Give the extent of all Babesia divergens-infected red blood cells.
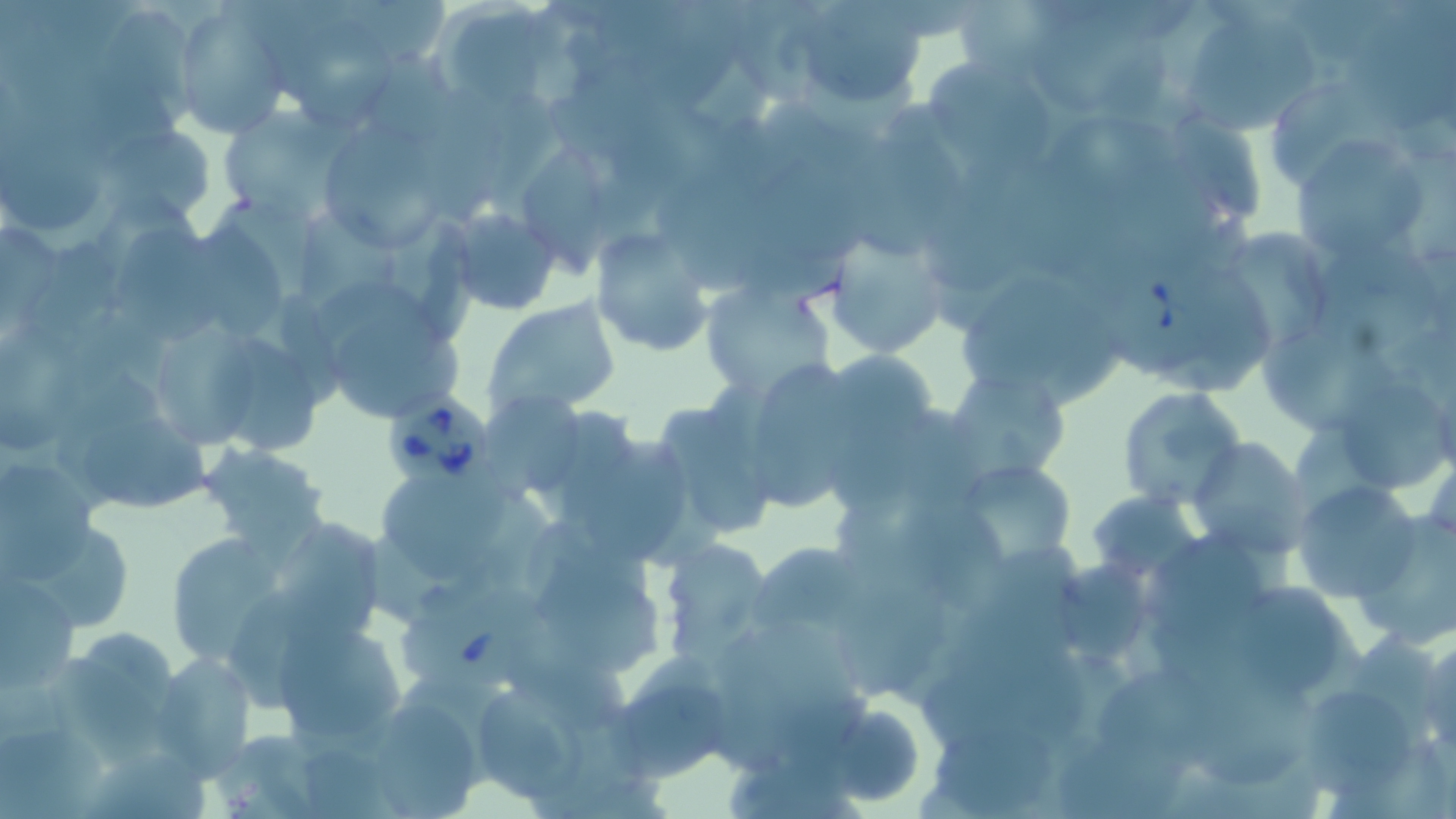

Approximate bounding boxes as (x1,y1)-(x2,y2) corner pairs in pixels.
Babesia divergens-infected red blood cells: (1097,249)-(1228,380), (384,386)-(497,495), (397,590)-(564,698).

Uninfected red blood cell locations: (788,1)-(930,111), (170,2)-(294,138), (433,2)-(565,110), (1181,4)-(1323,133), (102,6)-(203,132), (1038,18)-(1151,108), (277,19)-(405,128), (931,57)-(1055,178), (1272,79)-(1410,198), (218,106)-(340,225), (326,116)-(439,245), (103,123)-(219,228), (1288,135)-(1434,266), (521,144)-(611,284), (440,203)-(563,316), (300,207)-(399,347), (385,212)-(478,344), (118,224)-(219,347), (825,225)-(955,360), (589,228)-(718,359), (1237,228)-(1333,348), (1312,242)-(1446,355), (964,272)-(1095,390), (701,279)-(835,400), (484,297)-(622,421), (335,316)-(466,417), (1256,326)-(1396,434), (3,330)-(91,451), (160,330)-(261,447), (208,337)-(318,455), (819,348)-(942,453), (734,356)-(865,514), (943,363)-(1073,484), (1343,380)-(1449,487), (1116,386)-(1247,511), (486,397)-(587,492), (648,401)-(779,544), (83,416)-(219,509), (584,434)-(692,563), (1187,437)-(1312,558), (197,444)-(331,554), (952,458)-(1080,573), (0,461)-(96,581), (1291,478)-(1425,604), (381,479)-(517,578), (1087,491)-(1203,581), (903,495)-(1008,613), (1351,512)-(1456,644), (284,523)-(394,641), (38,529)-(135,628), (160,532)-(289,671), (1145,535)-(1271,640), (658,536)-(775,664), (748,541)-(877,646), (1061,561)-(1155,660), (535,563)-(668,671), (0,572)-(80,694), (1239,580)-(1345,691), (838,581)-(952,698), (276,617)-(407,750), (1418,631)-(1456,753), (152,652)-(257,776), (53,654)-(168,759), (611,657)-(736,784), (1103,670)-(1228,784), (1189,678)-(1330,797), (1304,689)-(1413,801), (477,694)-(587,802), (816,702)-(928,807), (377,705)-(478,819), (931,720)-(1067,819), (0,725)-(103,819), (88,749)-(223,819). Slide-level diagnosis: Babesia divergens. Single field of view. Optical microscopy. 1000x magnification. Image is 1456×819 pixels. Thin blood film. May-Grünwald-Giemsa stain.